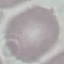

result = negative for malaria parasites
preparation = thin smear
capture = smartphone through the microscope eyepiece
image type = cell patch, automatically extracted from a larger field of view and resized to 64 × 64 pixels
stain = Giemsa